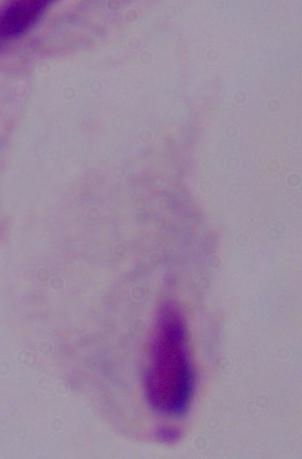 A trichomonad is seen. Micrograph. 1000x magnification.